State which cell type is depicted.
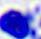

This is a leukocyte.

Captured at 400x magnification. Micrograph.